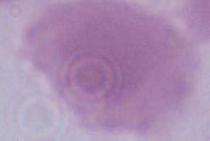

{
  "magnification": "1000x",
  "modality": "photomicrograph",
  "identification": "red blood cell"
}